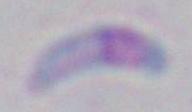 Micrograph. Toxoplasma gondii is seen. Captured at 1000x magnification.